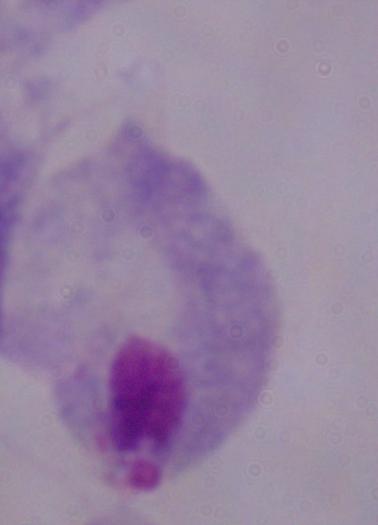
Summary:
  - Modality: micrograph
  - Identification: trichomonad
  - Magnification: 1000x